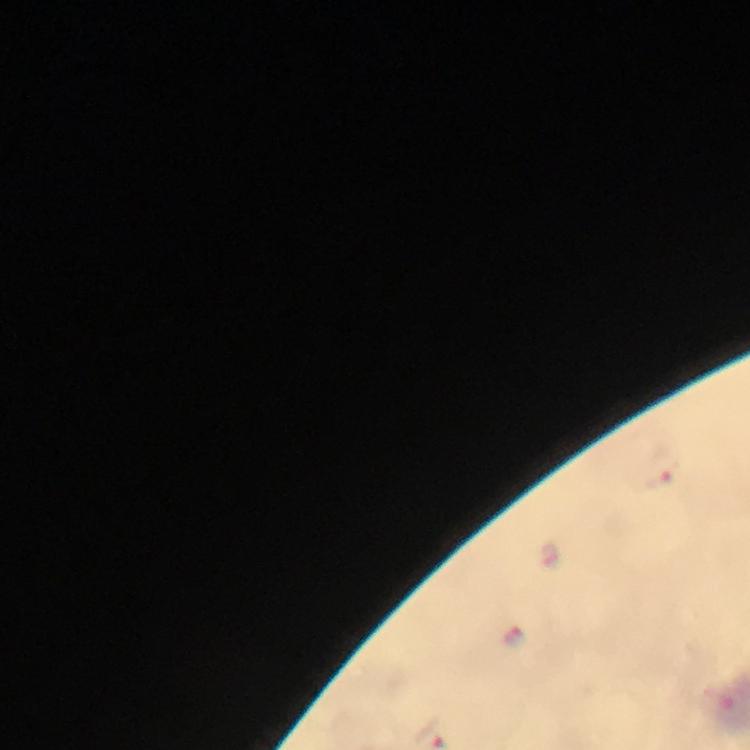
malaria parasite locations = approximate centers as {x, y} in pixels: {661, 472}, {547, 556}, {516, 636}
preparation = thick smear
context = from a malaria diagnostic workup
stain = Giemsa
image size = 750×750 pixels
magnification = 100x
immersion oil = used
capture = smartphone mounted on the microscope
cropped from = one field of view